Locate every leukocyte (white blood cell).
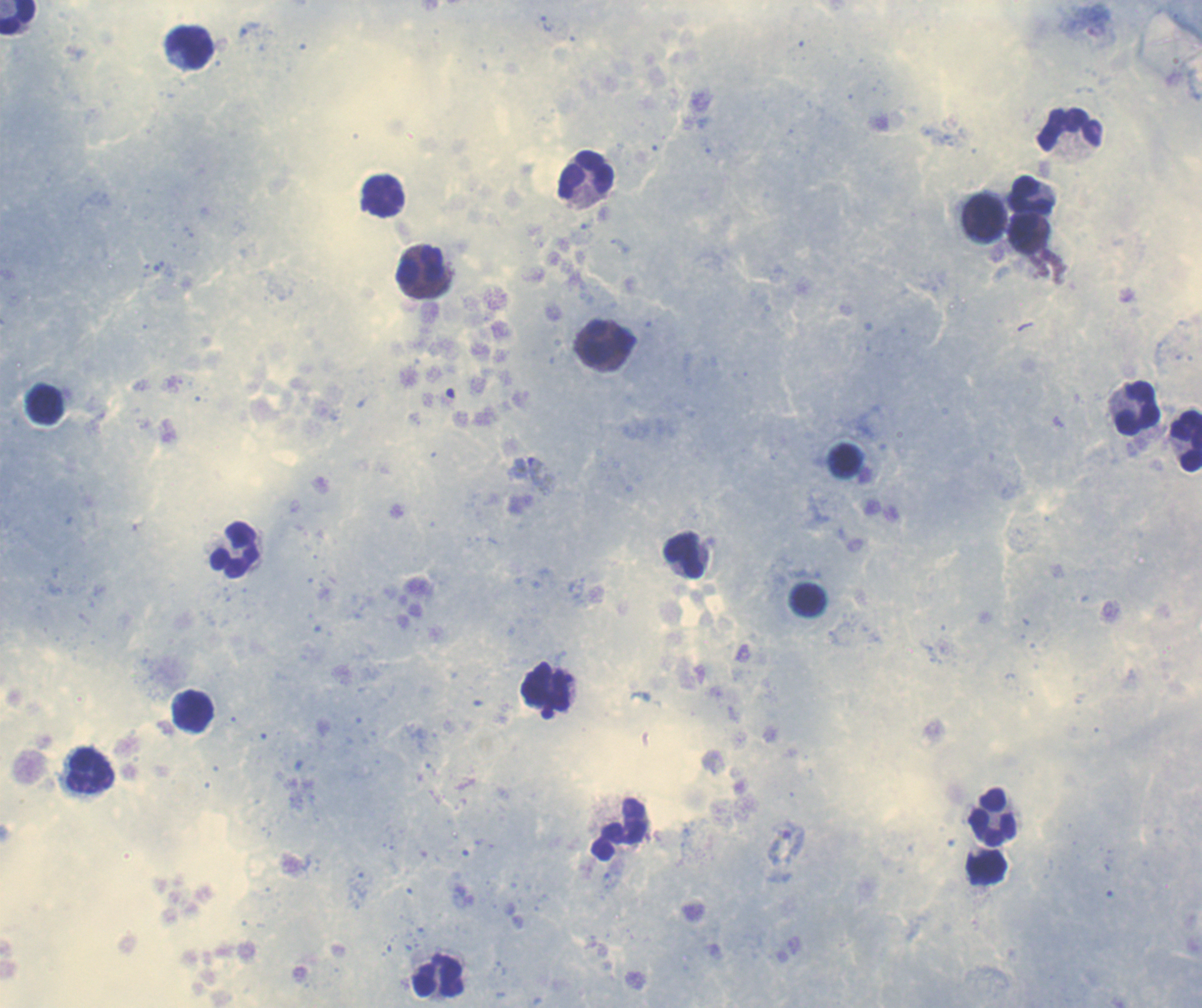
Approximate centers as {x, y} in pixels.
Leukocytes: {18, 17}, {191, 48}, {1070, 130}, {585, 175}, {1030, 196}, {385, 197}, {984, 217}, {1026, 234}, {420, 267}, {606, 341}, {45, 405}, {1137, 408}, {1186, 441}, {236, 549}, {684, 556}, {809, 600}, {547, 687}, {193, 713}, {91, 771}, {994, 816}, {438, 977}.

Approximate centers as {x, y} in pixels.
Summary:
  - Gametocyte locations: {785, 844}
  - Trophozoite locations: {546, 23}, {543, 476}
  - Life-cycle stages observed: trophozoite, gametocyte
  - Coloration quality: good
  - Background quality: good
  - Stain: Romanowsky
  - Context: previously used in an actual diagnosis
  - Field of view: single
  - Preparation: thick smear of blood
  - Magnification: 100x
  - Image size: 1202×1008 pixels
  - Result: positive for Plasmodium parasites